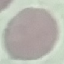

malaria status = uninfected
capture = smartphone camera at the microscope eyepiece
stain = Giemsa
preparation = thin blood smear
image type = automatically extracted cell patch, resized to 64 × 64 pixels